Assess this cell for malaria.
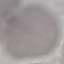

It is uninfected.

Photographed with a smartphone camera at the microscope eyepiece. Cell patch, automatically extracted from a larger field of view and resized to 64 × 64 pixels. Thin blood film. Giemsa-stained preparation.